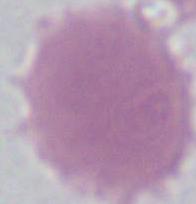
magnification = 1000x
identification = erythrocyte
modality = photomicrograph